Name the blood parasite species.
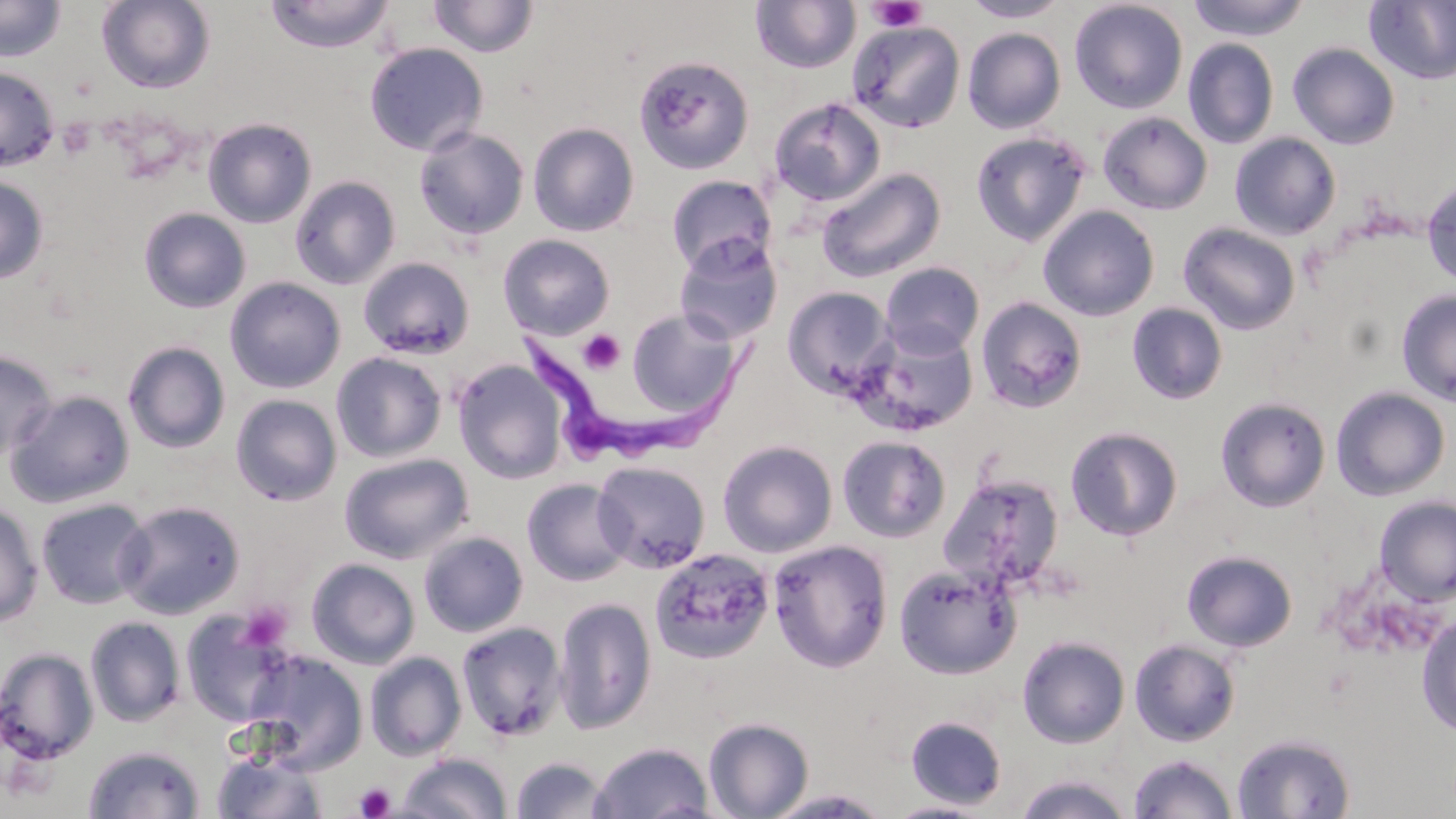

Trypanosoma brucei.

Summary:
  - Coordinate format: approximate bounding boxes as (x1,y1)-(x2,y2) corner pairs in pixels
  - Uninfected red blood cell locations: (0,0)-(66,62), (264,0)-(395,53), (427,0)-(540,58), (962,0)-(1070,22), (1069,0)-(1188,114), (1186,0)-(1311,42), (96,1)-(216,93), (750,1)-(861,75), (1364,1)-(1456,86), (846,21)-(965,133), (962,27)-(1066,134), (1183,38)-(1279,149), (364,42)-(489,156), (1287,42)-(1400,150), (634,55)-(755,175), (0,65)-(59,172), (769,97)-(885,206), (1097,111)-(1212,215), (203,117)-(317,228), (528,122)-(640,237), (413,126)-(530,241), (970,130)-(1091,246), (1230,132)-(1341,240), (816,167)-(946,283), (0,175)-(49,284), (666,175)-(777,275), (290,176)-(401,289), (1421,179)-(1456,288), (1038,205)-(1160,322), (138,208)-(251,313), (1177,221)-(1301,336), (674,233)-(784,346), (498,234)-(616,340), (358,256)-(475,359), (879,262)-(985,358), (224,277)-(346,394), (782,286)-(896,400), (1395,289)-(1456,407), (975,296)-(1088,414), (1127,302)-(1228,405), (626,307)-(741,417), (854,324)-(979,436), (122,341)-(232,453), (0,350)-(58,460), (331,351)-(447,463), (452,359)-(569,484), (1330,386)-(1450,501), (5,390)-(136,508), (230,394)-(342,506), (1215,397)-(1331,512), (1065,426)-(1184,541), (837,435)-(951,542), (717,440)-(838,558), (339,452)-(474,564), (592,460)-(711,574), (938,473)-(1064,595), (521,478)-(632,586), (1373,496)-(1456,606), (35,497)-(153,610), (0,500)-(44,628), (115,500)-(246,619), (418,530)-(528,637), (767,538)-(894,673), (649,547)-(775,664), (1181,549)-(1298,652), (306,558)-(420,669), (893,562)-(1020,680), (553,596)-(657,735), (181,609)-(295,727), (1416,614)-(1456,738), (84,616)-(186,727), (455,620)-(569,741), (1016,635)-(1130,748), (1129,638)-(1241,747), (0,646)-(99,764), (243,651)-(368,774), (364,651)-(466,761), (905,715)-(1008,809), (703,717)-(814,819), (1232,732)-(1357,818), (590,741)-(714,819), (82,744)-(205,819), (212,747)-(327,818), (397,752)-(512,818), (1127,753)-(1238,819), (510,756)-(612,818), (1014,773)-(1133,819), (764,788)-(893,818), (883,800)-(993,818)
  - Trypanosoma brucei locations: (516,321)-(767,477)
  - Platelet locations: (867,1)-(927,32), (577,329)-(625,376), (237,602)-(290,651), (353,782)-(396,818)
  - Image size: 1456×819 pixels
  - Magnification: 1000x
  - Preparation: thin blood film
  - Field of view: single
  - Stain: May-Grünwald-Giemsa
  - Modality: optical microscopy